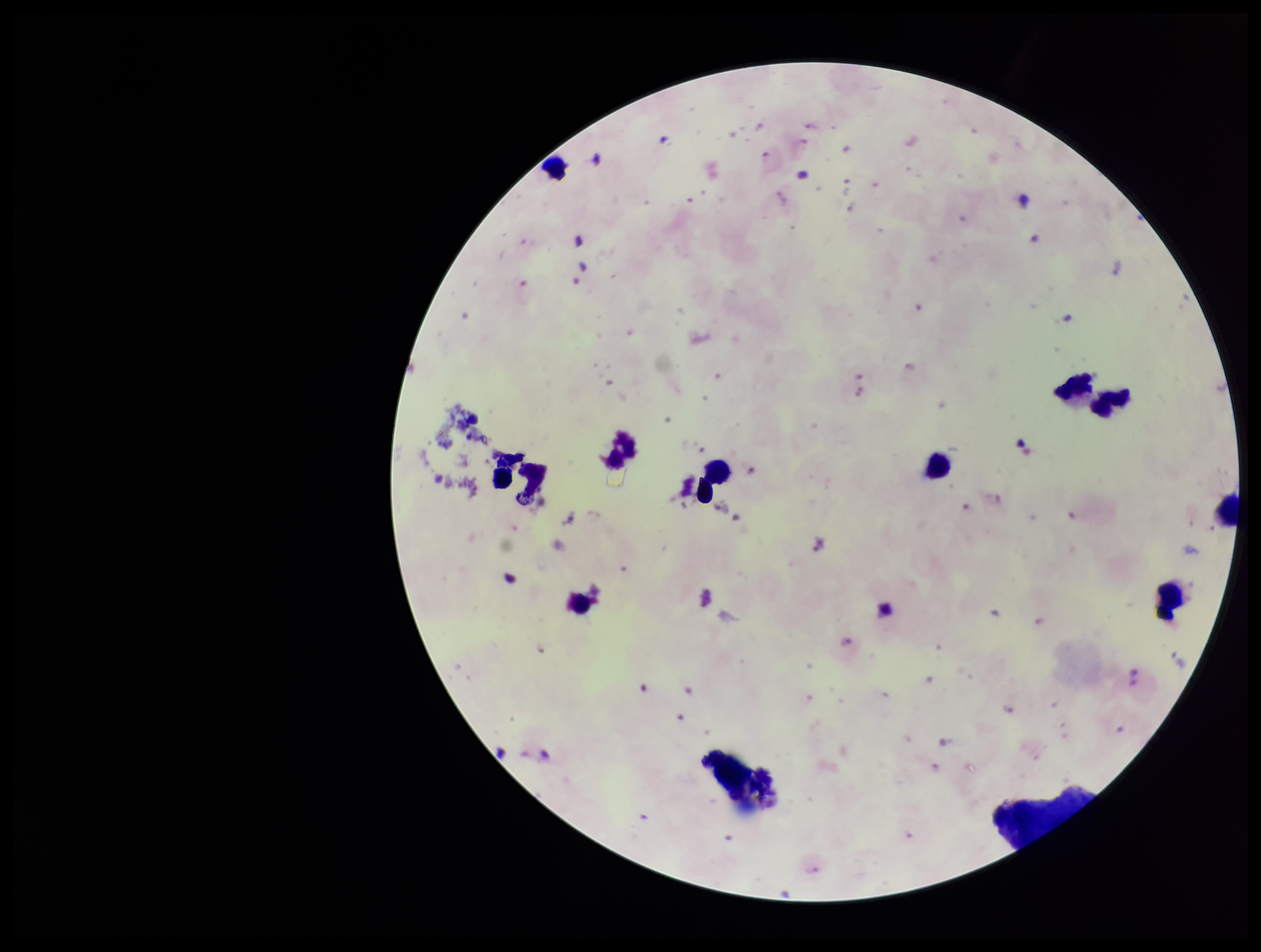

Summary:
  - Field of view: one from this slide
  - Image size: 1261×952 pixels
  - Leukocyte count: 11
  - Parasite count: 11
  - Plasmodium parasites: detected
  - Species reported for this patient: Plasmodium falciparum
  - Stain: Giemsa
  - Preparation: thick blood smear
  - Patient malaria status: infected
  - Capture: smartphone photograph through the microscope eyepiece